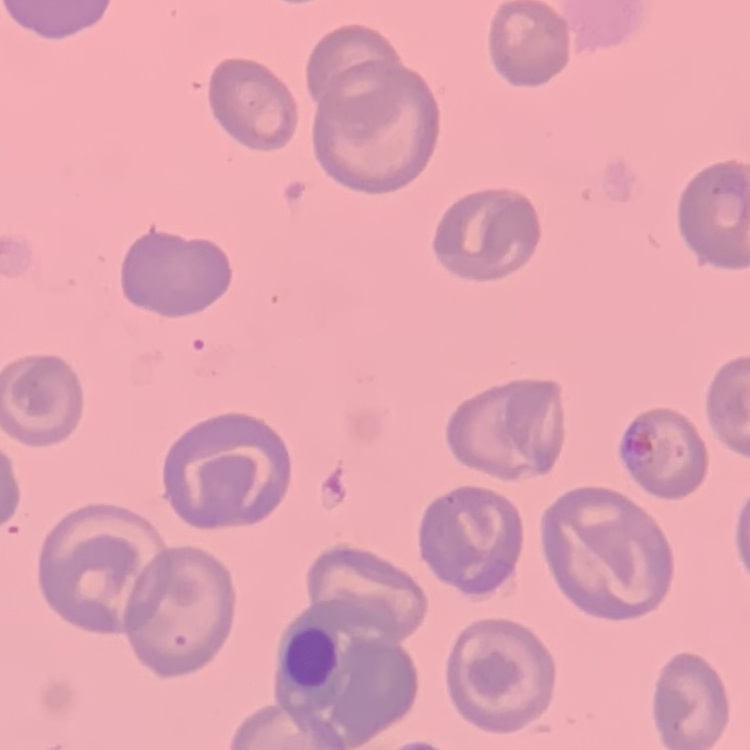
erythrocyte morphology = no rouleaux formation
preparation = thin peripheral smear
stain = Field's or Giemsa
image type = square crop of a larger photomicrograph